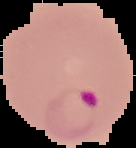

Segmented cell region on a black background. From a thin blood smear. Malaria status: parasitized. Image is 136×148 pixels.